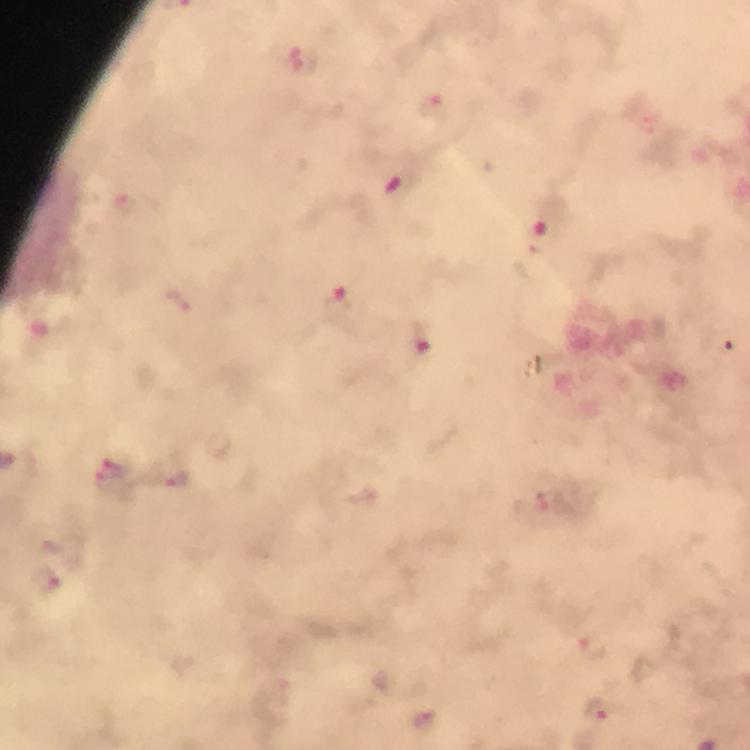
context = from a diagnostic examination for malaria
magnification = 100x
immersion oil = applied
malaria parasite locations = approximate centers as {x, y} in pixels: {432, 105}, {395, 186}, {542, 234}, {335, 298}, {420, 341}, {111, 474}, {175, 479}, {45, 579}, {592, 646}, {598, 709}, {423, 719}
capture = smartphone mounted on the microscope
cropped from = one field of view
preparation = thick blood film
image size = 750×750 pixels
stain = Giemsa